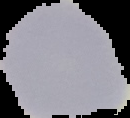 From a thin blood smear. Malaria status: uninfected. The area outside the segmented cell region is set to black. Image is 130×118 pixels.